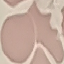

malaria_status: uninfected
image_type: cell patch, automatically extracted from a larger field of view and resized to 64 × 64 pixels
preparation: thin smear
stain: Giemsa
capture: smartphone camera at the microscope eyepiece